Give the position of every Plasmodium parasite.
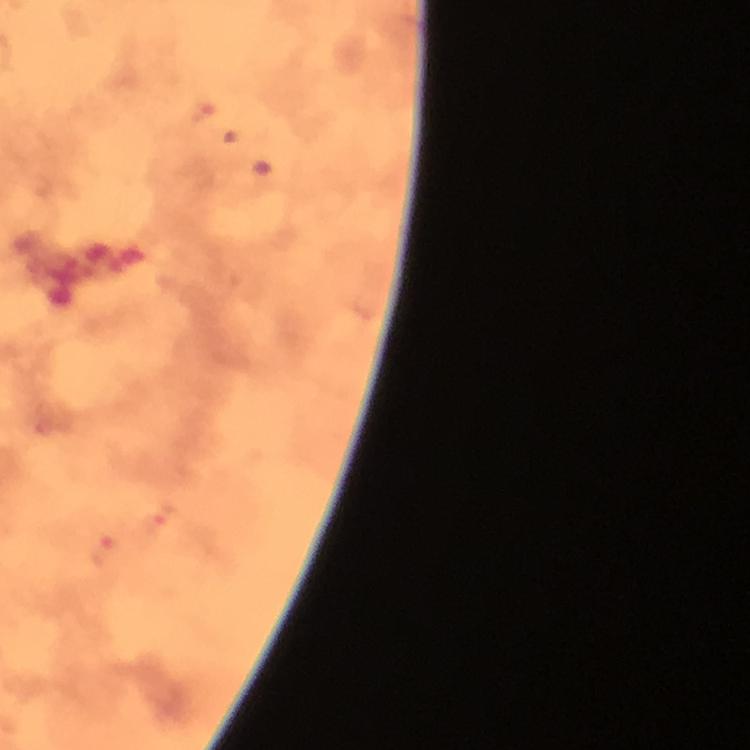

Approximate object centers, in pixels from the top-left corner.
Plasmodium parasites: (x=201, y=111), (x=237, y=132), (x=262, y=176), (x=158, y=520), (x=104, y=554).

capture = smartphone camera through the microscope
image size = 750×750 pixels
immersion oil = used
magnification = 100x
cropped from = a single field of view
context = from a diagnostic examination for malaria
preparation = thick smear
stain = Giemsa